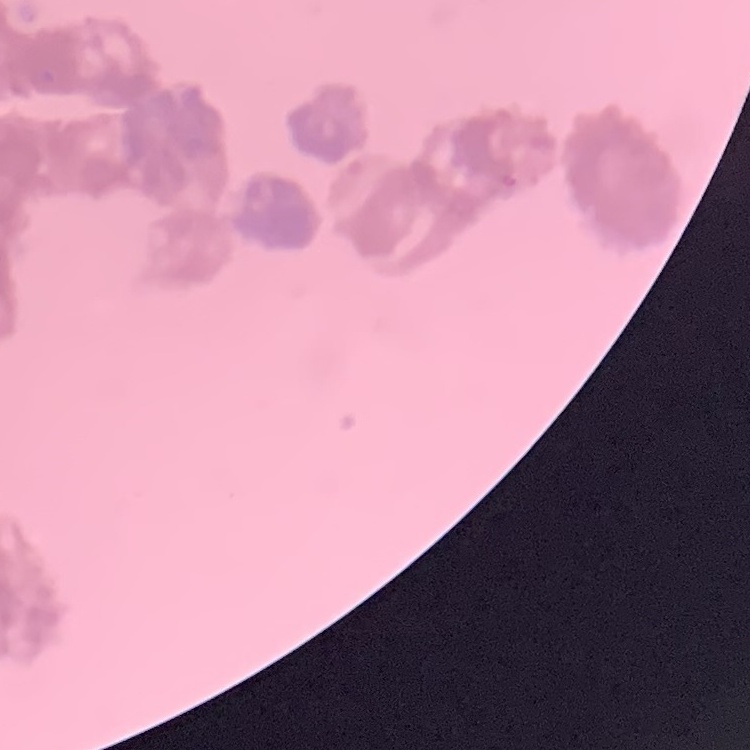
The red blood cells show rouleaux formation. Square crop of a larger photomicrograph. Field's or Giemsa stain. Thin blood smear.